Report the malaria status of this cell.
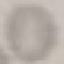
It is uninfected.

capture = smartphone through the microscope eyepiece
stain = Giemsa
image type = automatically extracted cell patch, resized to 64 × 64 pixels
preparation = thin blood film